Assess this cell for malaria.
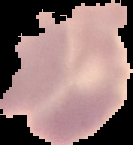
Uninfected.

Summary:
  - Image size: 133×145 pixels
  - Preparation: thin blood smear
  - Image type: segmented cell region with the area outside set to black